Give the extent of all Plasmodium ovale-infected red blood cells.
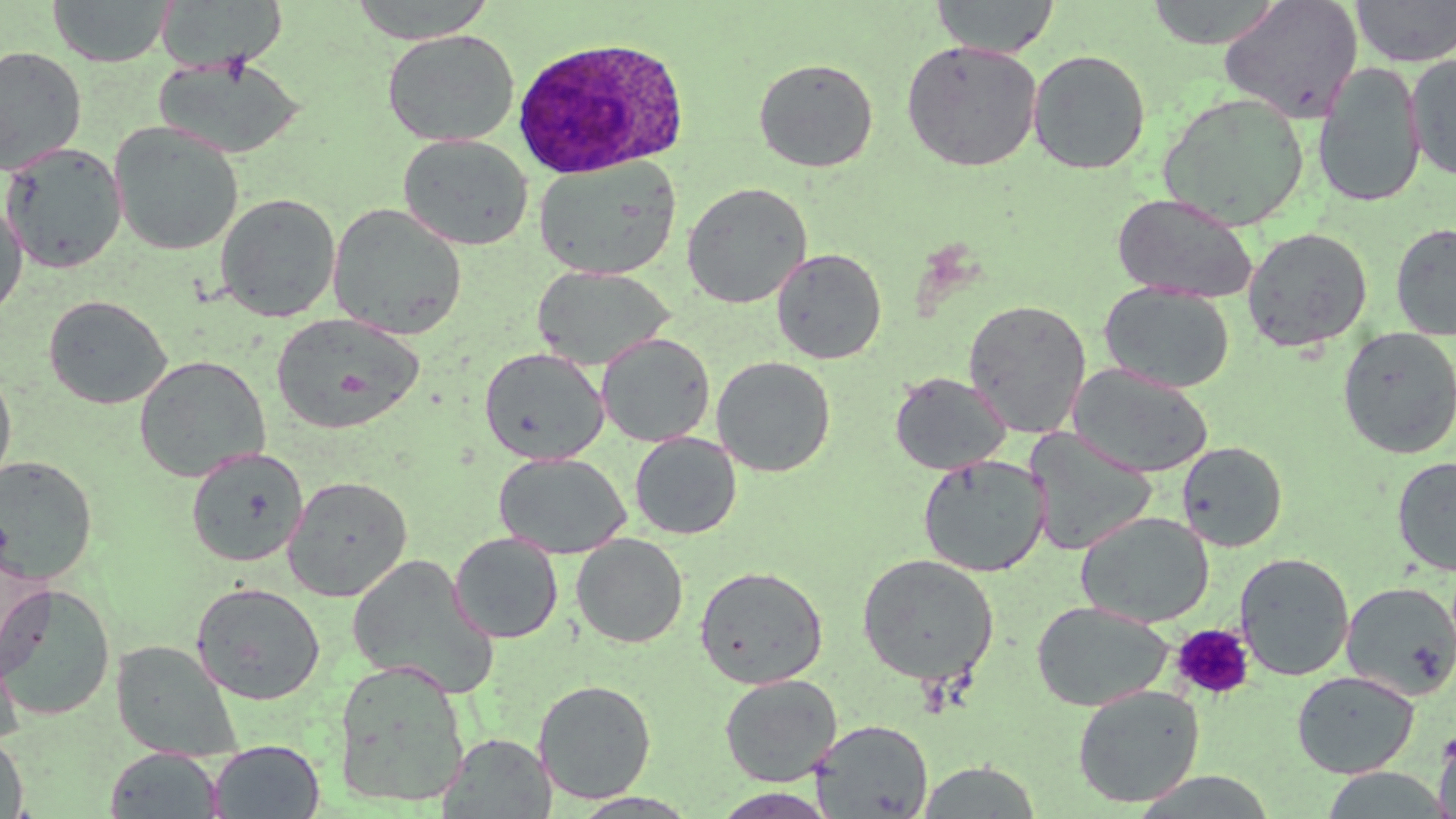
Approximate bounding boxes as named x1/y1/x2/y2 corners in pixels.
Plasmodium ovale-infected red blood cells: (x1=510, y1=36, x2=690, y2=179).

Uninfected red blood cell locations: (x1=47, y1=0, x2=176, y2=67), (x1=157, y1=0, x2=289, y2=72), (x1=347, y1=0, x2=498, y2=43), (x1=929, y1=0, x2=1060, y2=58), (x1=1145, y1=0, x2=1284, y2=49), (x1=1218, y1=0, x2=1363, y2=123), (x1=1350, y1=0, x2=1456, y2=67), (x1=382, y1=29, x2=520, y2=147), (x1=901, y1=40, x2=1042, y2=172), (x1=0, y1=45, x2=88, y2=176), (x1=1027, y1=49, x2=1151, y2=174), (x1=1405, y1=53, x2=1456, y2=180), (x1=152, y1=57, x2=305, y2=159), (x1=753, y1=57, x2=879, y2=173), (x1=1313, y1=62, x2=1427, y2=209), (x1=1157, y1=92, x2=1310, y2=231), (x1=109, y1=122, x2=244, y2=256), (x1=398, y1=134, x2=533, y2=251), (x1=1, y1=142, x2=127, y2=274), (x1=534, y1=156, x2=682, y2=280), (x1=681, y1=182, x2=813, y2=308), (x1=1112, y1=192, x2=1259, y2=303), (x1=215, y1=193, x2=341, y2=322), (x1=0, y1=196, x2=28, y2=321), (x1=327, y1=202, x2=468, y2=341), (x1=1390, y1=223, x2=1456, y2=340), (x1=1242, y1=227, x2=1373, y2=352), (x1=771, y1=247, x2=887, y2=364), (x1=533, y1=265, x2=675, y2=370), (x1=1100, y1=282, x2=1235, y2=393), (x1=43, y1=295, x2=172, y2=409), (x1=962, y1=298, x2=1091, y2=438), (x1=271, y1=312, x2=425, y2=434), (x1=1336, y1=327, x2=1456, y2=459), (x1=596, y1=333, x2=715, y2=447), (x1=479, y1=347, x2=609, y2=465), (x1=134, y1=355, x2=270, y2=481), (x1=712, y1=355, x2=836, y2=477), (x1=0, y1=363, x2=17, y2=495), (x1=1069, y1=363, x2=1214, y2=478), (x1=889, y1=371, x2=1011, y2=475), (x1=1024, y1=429, x2=1157, y2=555), (x1=629, y1=432, x2=742, y2=540), (x1=1176, y1=441, x2=1287, y2=552), (x1=186, y1=447, x2=309, y2=567), (x1=493, y1=452, x2=630, y2=559), (x1=917, y1=454, x2=1050, y2=577), (x1=0, y1=455, x2=98, y2=585), (x1=1392, y1=455, x2=1456, y2=577), (x1=283, y1=475, x2=413, y2=602), (x1=1076, y1=511, x2=1214, y2=627), (x1=449, y1=533, x2=563, y2=643), (x1=572, y1=533, x2=688, y2=648), (x1=0, y1=542, x2=50, y2=679), (x1=1234, y1=552, x2=1354, y2=681), (x1=857, y1=553, x2=1000, y2=685), (x1=347, y1=554, x2=499, y2=698), (x1=694, y1=565, x2=828, y2=688), (x1=190, y1=581, x2=326, y2=705), (x1=1341, y1=581, x2=1456, y2=700), (x1=0, y1=584, x2=116, y2=721), (x1=1031, y1=600, x2=1173, y2=711), (x1=0, y1=628, x2=24, y2=749), (x1=111, y1=640, x2=243, y2=761), (x1=334, y1=660, x2=470, y2=808), (x1=1291, y1=670, x2=1420, y2=778), (x1=719, y1=674, x2=842, y2=786), (x1=533, y1=679, x2=657, y2=803), (x1=1072, y1=684, x2=1205, y2=808), (x1=810, y1=719, x2=933, y2=818), (x1=1432, y1=726, x2=1456, y2=819), (x1=0, y1=732, x2=29, y2=819), (x1=439, y1=733, x2=555, y2=818), (x1=208, y1=740, x2=324, y2=819), (x1=105, y1=747, x2=224, y2=818), (x1=915, y1=760, x2=1043, y2=818), (x1=1319, y1=768, x2=1455, y2=818), (x1=711, y1=788, x2=839, y2=818), (x1=568, y1=792, x2=701, y2=818). Platelet locations: (x1=1170, y1=623, x2=1254, y2=701). Slide-level diagnosis: Plasmodium ovale. 1000x magnification. Thin blood smear. May-Grünwald-Giemsa stain. Single field of view. Image is 1456×819 pixels. Light microscopy.